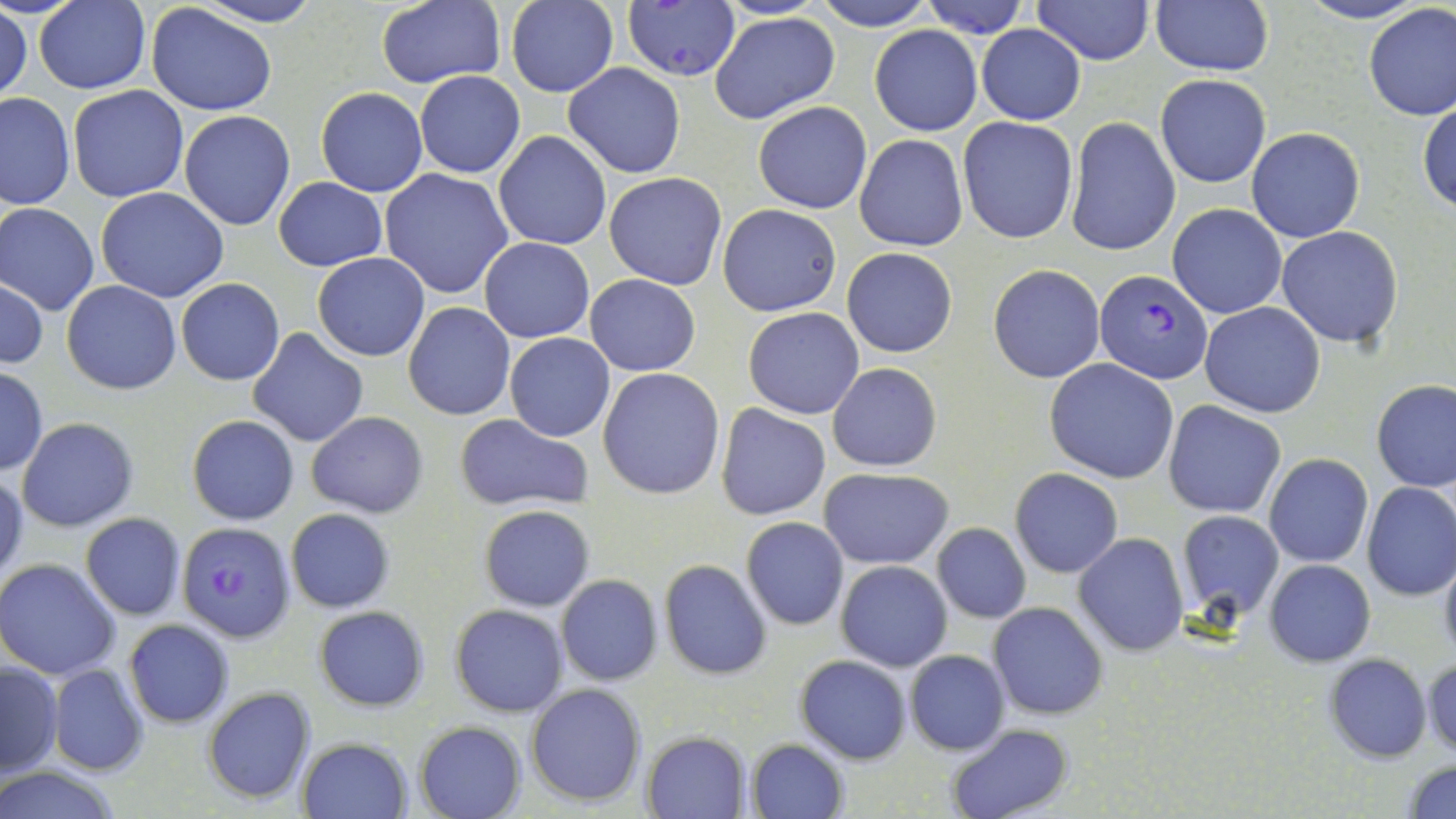
Summary:
  - Coordinate format: approximate bounding boxes as [x1, y1, x2, y2] in pixels
  - Uninfected red blood cell locations: [375, 0, 506, 90], [506, 0, 618, 96], [814, 0, 938, 30], [919, 0, 1030, 36], [1032, 0, 1153, 64], [1298, 0, 1428, 25], [33, 1, 150, 93], [193, 1, 323, 27], [1150, 2, 1273, 76], [1362, 3, 1456, 120], [147, 4, 277, 115], [1, 6, 32, 107], [710, 12, 839, 124], [869, 25, 982, 135], [976, 25, 1085, 125], [564, 63, 686, 178], [414, 69, 526, 178], [1154, 72, 1271, 189], [68, 85, 191, 203], [315, 87, 427, 197], [0, 92, 74, 210], [77, 96, 288, 214], [754, 100, 871, 212], [1418, 101, 1456, 215], [179, 109, 295, 231], [956, 115, 1079, 245], [1066, 116, 1180, 257], [1246, 128, 1364, 244], [493, 131, 613, 250], [854, 134, 967, 251], [380, 168, 513, 300], [604, 171, 727, 289], [275, 177, 387, 272], [96, 186, 228, 303], [1168, 203, 1288, 319], [1, 204, 100, 315], [717, 204, 842, 316], [1276, 226, 1404, 348], [478, 237, 595, 343], [842, 247, 957, 358], [313, 251, 430, 361], [988, 264, 1104, 384], [585, 274, 701, 377], [1, 279, 47, 368], [176, 279, 285, 385], [62, 280, 180, 395], [403, 301, 516, 420], [1200, 302, 1327, 417], [744, 307, 864, 420], [248, 327, 368, 448], [504, 333, 615, 441], [1046, 358, 1180, 483], [827, 362, 942, 472], [0, 367, 47, 475], [598, 367, 726, 500], [1371, 379, 1455, 492], [1164, 401, 1286, 518], [716, 405, 831, 519], [306, 411, 428, 518], [187, 414, 300, 525], [454, 414, 593, 514], [17, 418, 139, 533], [1265, 453, 1373, 568], [819, 468, 953, 568], [1011, 468, 1122, 578], [0, 470, 28, 589], [1362, 483, 1456, 600], [479, 504, 595, 612], [285, 508, 395, 612], [1176, 509, 1284, 621], [81, 513, 185, 620], [741, 517, 849, 631], [931, 523, 1031, 624], [1073, 532, 1190, 657], [1439, 549, 1456, 665], [0, 559, 121, 679], [659, 559, 773, 680], [1264, 559, 1375, 666], [836, 560, 953, 671], [555, 574, 664, 687], [989, 602, 1108, 719], [450, 604, 567, 716], [314, 606, 429, 712], [123, 619, 235, 729], [906, 650, 1010, 756], [1323, 653, 1432, 762], [794, 654, 911, 764], [1422, 657, 1455, 760], [1, 660, 63, 778], [49, 663, 150, 777], [525, 682, 648, 807], [202, 686, 316, 805], [414, 720, 526, 819], [947, 724, 1072, 818], [643, 732, 751, 818], [297, 737, 412, 818], [747, 739, 848, 818], [1403, 760, 1456, 817], [0, 762, 125, 819]
  - Plasmodium falciparum-infected red blood cell locations: [621, 3, 741, 82], [1095, 269, 1213, 384], [178, 522, 295, 644]
  - Slide-level diagnosis: Plasmodium falciparum
  - Preparation: thin blood smear
  - Magnification: 1000x
  - Stain: May-Grünwald-Giemsa
  - Field of view: single
  - Image size: 1456×819 pixels
  - Modality: optical microscopy